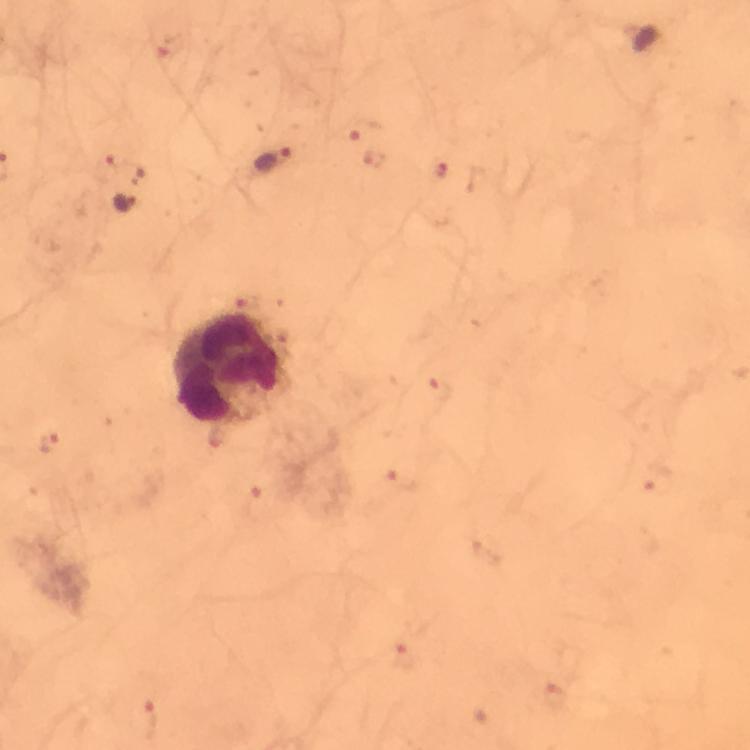

Approximate centers as (x, y) in pixels. Leukocyte locations: (229, 370). Plasmodium parasite locations: (361, 128), (375, 160), (276, 162), (105, 168), (442, 169), (125, 202), (440, 391), (217, 438), (50, 444), (658, 480), (401, 483), (259, 502), (408, 657), (556, 693), (147, 720). Immersion oil applied. Cropped region of a single field of view. Giemsa-stained preparation. At 100x magnification. From a diagnostic examination for malaria. Thick blood film. Image is 750×750 pixels. Smartphone photograph taken through a microscope.